Locate every Plasmodium parasite.
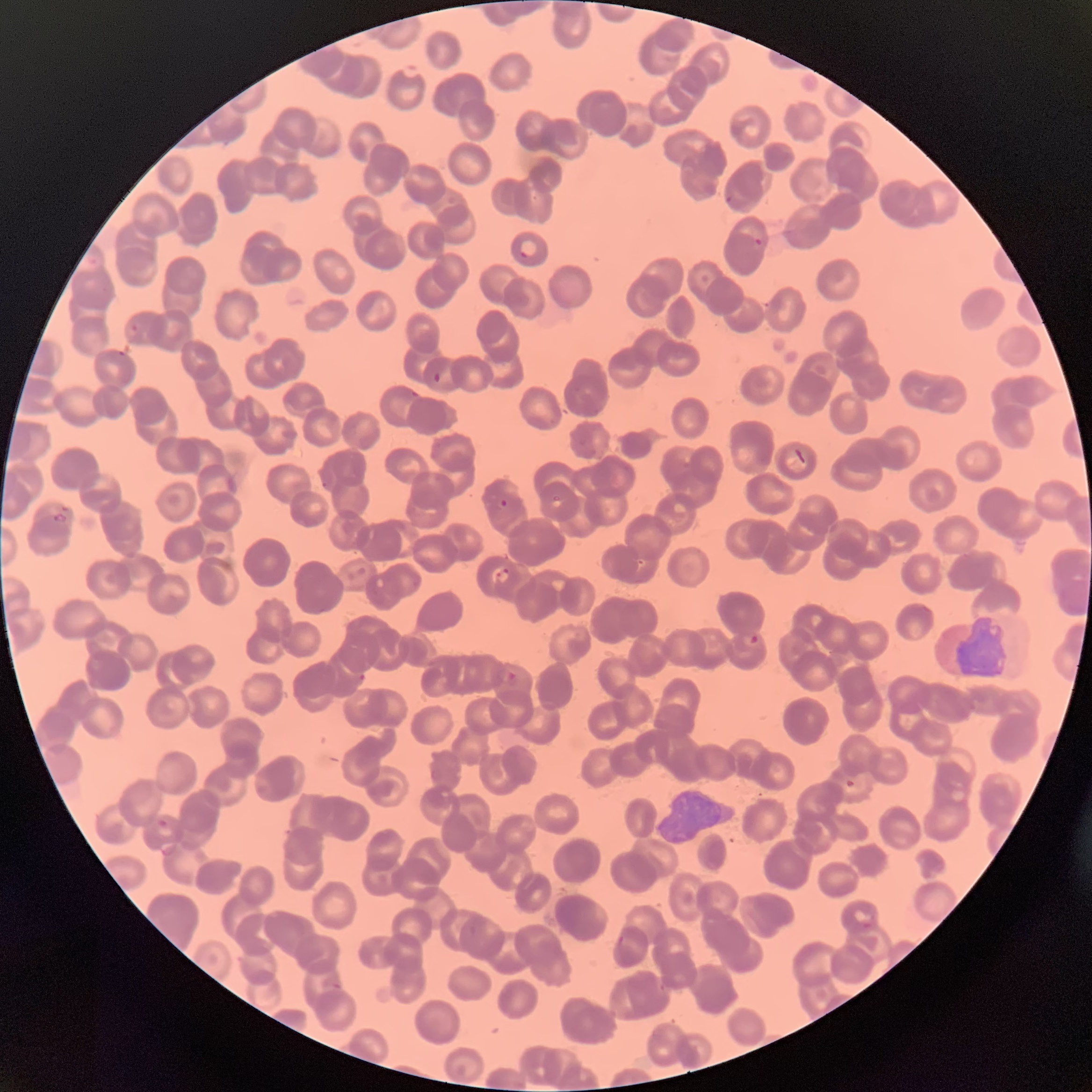

Approximate bounding boxes as [x1, y1, x2, y2] in pixels.
Plasmodium parasites: [725, 194, 733, 205], [754, 236, 763, 248], [518, 238, 538, 259], [127, 324, 140, 337], [118, 350, 128, 358], [432, 371, 443, 385], [410, 389, 421, 398], [322, 481, 330, 489], [497, 498, 509, 509], [52, 513, 68, 524], [493, 567, 511, 583], [744, 634, 761, 650], [498, 668, 517, 683], [357, 672, 366, 683], [844, 779, 859, 788], [156, 818, 174, 837], [852, 909, 877, 930], [617, 933, 627, 947].

{
  "red_blood_cell_morphology": "rouleaux formation",
  "modality": "light microscopy",
  "image_size": "1092×1092 pixels",
  "preparation": "thin blood film"
}